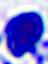

{
  "modality": "photomicrograph",
  "identification": "leukocyte",
  "magnification": "400x"
}